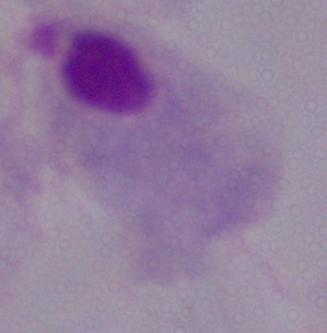

Micrograph. A trichomonad is seen. Captured at 1000x magnification.